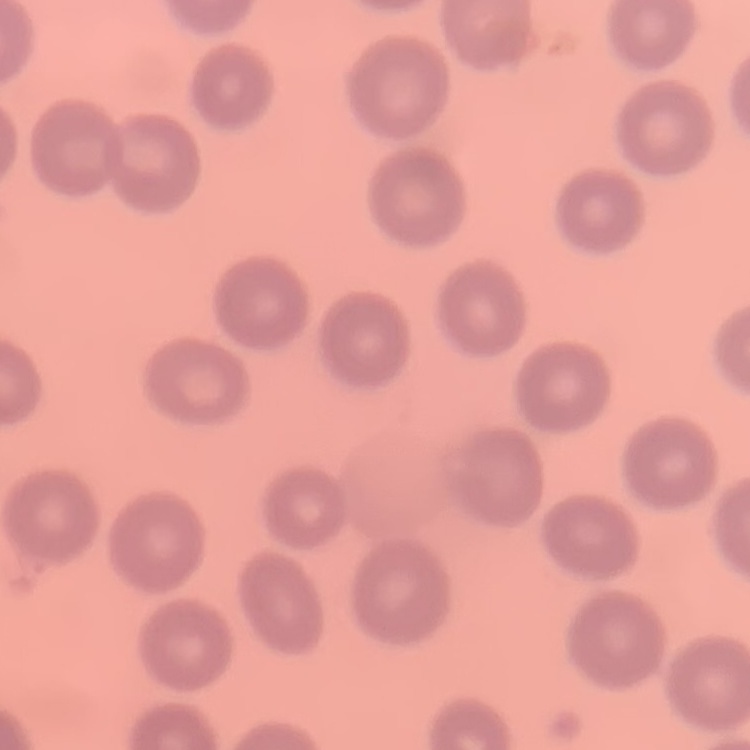
Summary:
  - Red blood cell morphology: no rouleaux formation
  - Image type: one tile cut from a larger photomicrograph
  - Preparation: thin blood smear
  - Stain: Field's or Giemsa